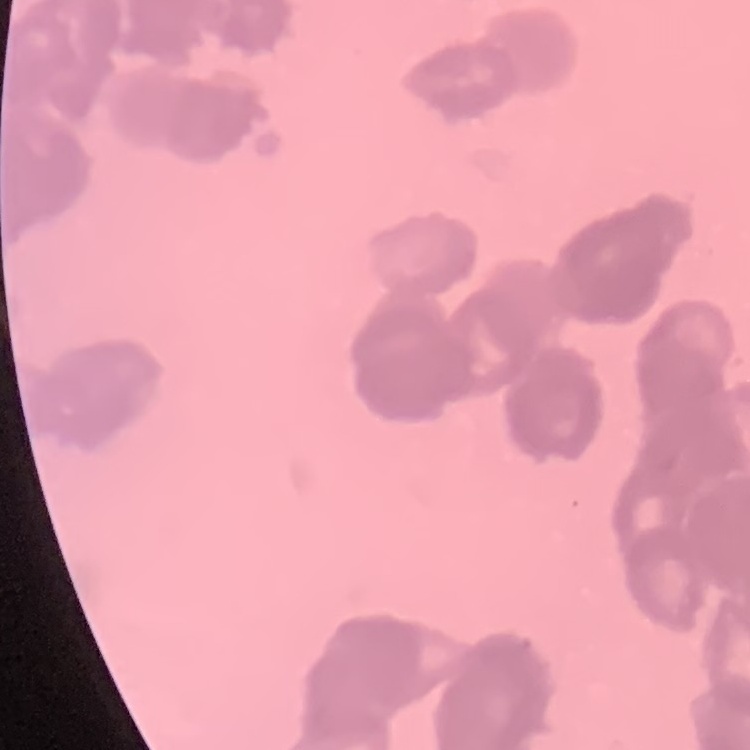
red blood cell morphology = rouleaux formation
preparation = thin blood film
stain = Field's or Giemsa
image type = square crop of a larger photomicrograph